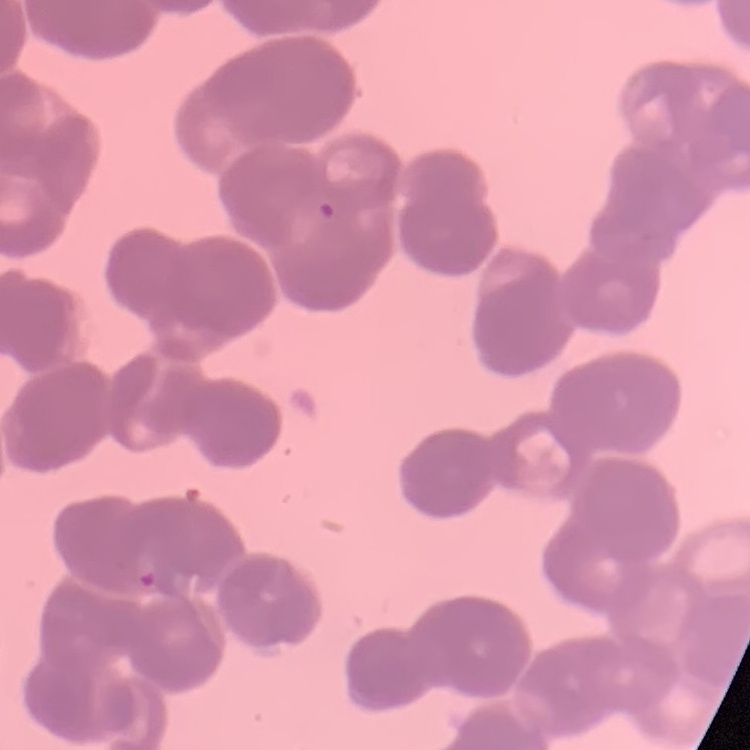

The red blood cells exhibit rouleaux formation. Thin blood smear. One tile cut from a larger photomicrograph. Stained with either Field's or Giemsa.